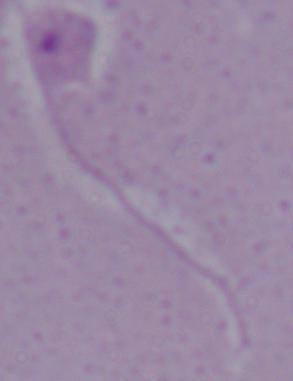 A Leishmania parasite is shown. Photomicrograph. 1000x magnification.